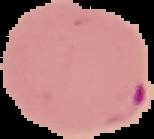
Segmented cell region on a black background. From a thin blood smear. Malaria status: parasitized. Image is 154×139 pixels.